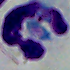
modality = micrograph
magnification = 1000x
identification = white blood cell